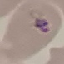 Malaria status: parasitized. Giemsa stain. Photographed with a smartphone camera at the microscope eyepiece. Cell patch, automatically extracted from a larger field of view and resized to 64 × 64 pixels. Thin smear of blood.